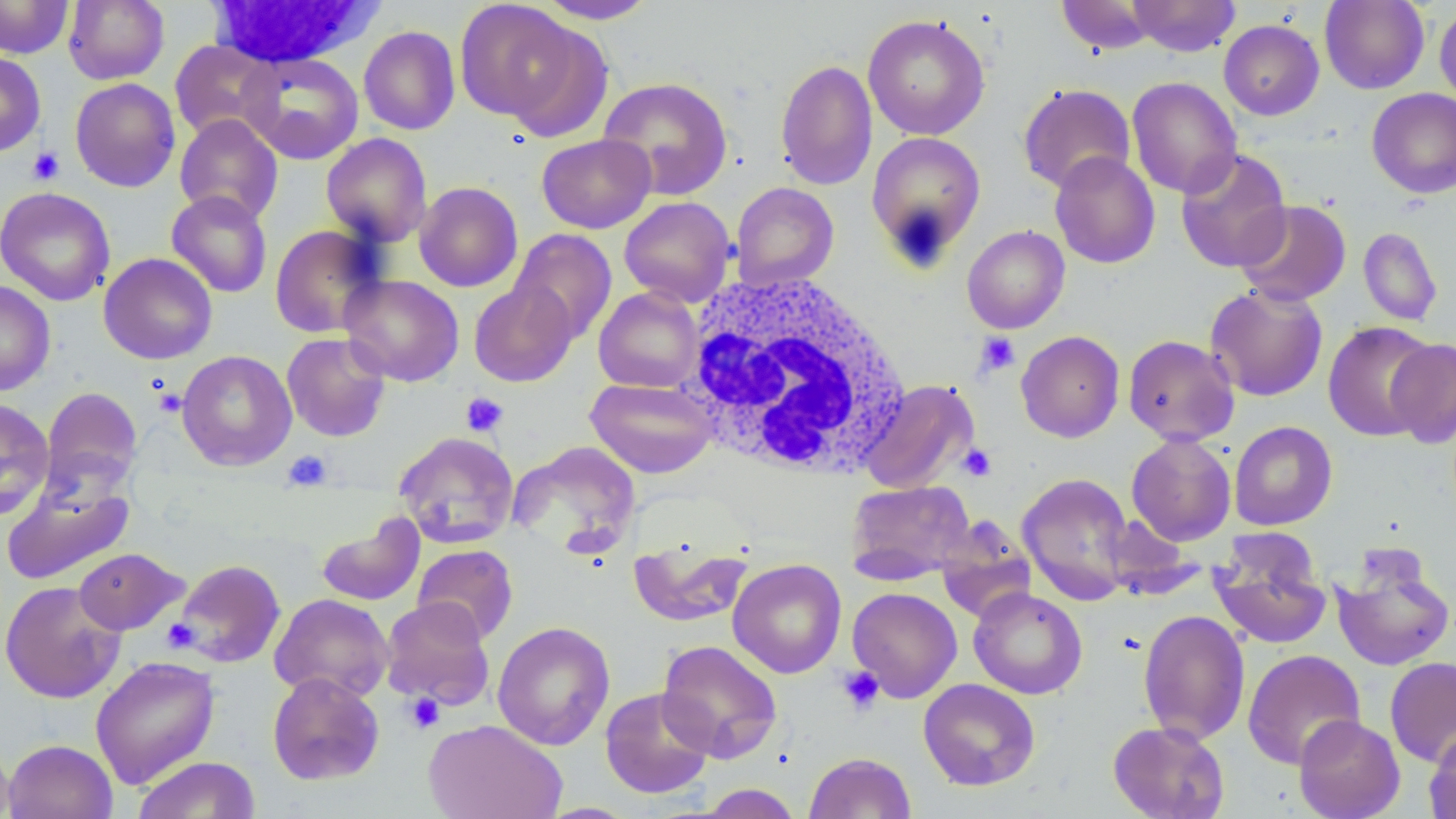

slide_level_diagnosis: no evidence of blood parasites
stain: May-Grünwald-Giemsa
magnification: 1000x
white_blood_cell_locations: 'approximate bounding boxes as named x1/y1/x2/y2 corners in pixels: (x1=206, y1=0, x2=381, y2=69), (x1=680, y1=272, x2=913, y2=480)'
uninfected_red_blood_cell_locations: 'approximate bounding boxes as named x1/y1/x2/y2 corners in pixels: (x1=0, y1=0, x2=73, y2=58), (x1=63, y1=0, x2=169, y2=85), (x1=455, y1=0, x2=581, y2=122), (x1=1056, y1=0, x2=1157, y2=55), (x1=1127, y1=0, x2=1240, y2=57), (x1=1319, y1=0, x2=1430, y2=94), (x1=535, y1=1, x2=659, y2=24), (x1=1434, y1=5, x2=1456, y2=107), (x1=863, y1=13, x2=990, y2=140), (x1=358, y1=17, x2=568, y2=128), (x1=500, y1=17, x2=614, y2=144), (x1=1219, y1=19, x2=1324, y2=120), (x1=358, y1=26, x2=460, y2=135), (x1=169, y1=40, x2=279, y2=143), (x1=0, y1=51, x2=46, y2=157), (x1=240, y1=52, x2=364, y2=164), (x1=775, y1=59, x2=878, y2=190), (x1=598, y1=76, x2=733, y2=200), (x1=69, y1=77, x2=181, y2=192), (x1=1127, y1=77, x2=1242, y2=199), (x1=1017, y1=83, x2=1136, y2=194), (x1=1366, y1=88, x2=1456, y2=198), (x1=174, y1=113, x2=283, y2=225), (x1=865, y1=130, x2=986, y2=264), (x1=321, y1=132, x2=432, y2=247), (x1=536, y1=134, x2=655, y2=233), (x1=1175, y1=148, x2=1292, y2=273), (x1=1049, y1=151, x2=1160, y2=269), (x1=414, y1=181, x2=523, y2=292), (x1=731, y1=182, x2=839, y2=290), (x1=0, y1=187, x2=115, y2=306), (x1=166, y1=190, x2=272, y2=297), (x1=619, y1=196, x2=737, y2=307), (x1=1234, y1=199, x2=1352, y2=306), (x1=270, y1=224, x2=385, y2=338), (x1=962, y1=225, x2=1070, y2=333), (x1=1358, y1=227, x2=1443, y2=326), (x1=509, y1=228, x2=618, y2=344), (x1=98, y1=253, x2=218, y2=364), (x1=339, y1=274, x2=464, y2=387), (x1=0, y1=280, x2=55, y2=396), (x1=469, y1=281, x2=578, y2=387), (x1=1205, y1=283, x2=1328, y2=402), (x1=593, y1=287, x2=704, y2=392), (x1=1322, y1=320, x2=1438, y2=442), (x1=1016, y1=331, x2=1125, y2=443), (x1=281, y1=332, x2=391, y2=442), (x1=1123, y1=334, x2=1240, y2=446), (x1=1386, y1=337, x2=1456, y2=448), (x1=177, y1=350, x2=297, y2=470), (x1=585, y1=377, x2=718, y2=478), (x1=859, y1=379, x2=979, y2=494), (x1=40, y1=386, x2=142, y2=500), (x1=0, y1=398, x2=54, y2=521), (x1=1229, y1=421, x2=1338, y2=530), (x1=393, y1=431, x2=520, y2=548), (x1=1126, y1=433, x2=1237, y2=546), (x1=508, y1=440, x2=641, y2=555), (x1=1017, y1=473, x2=1135, y2=605), (x1=846, y1=480, x2=975, y2=584), (x1=1, y1=481, x2=135, y2=586), (x1=316, y1=513, x2=425, y2=606), (x1=936, y1=518, x2=1036, y2=623), (x1=1210, y1=537, x2=1332, y2=650), (x1=629, y1=538, x2=751, y2=627), (x1=412, y1=544, x2=519, y2=644), (x1=73, y1=547, x2=188, y2=635), (x1=1331, y1=553, x2=1455, y2=672), (x1=728, y1=558, x2=847, y2=678), (x1=172, y1=559, x2=286, y2=669), (x1=0, y1=581, x2=125, y2=704), (x1=847, y1=587, x2=963, y2=703), (x1=968, y1=587, x2=1088, y2=699), (x1=269, y1=593, x2=394, y2=702), (x1=380, y1=597, x2=495, y2=710), (x1=1138, y1=609, x2=1250, y2=745), (x1=492, y1=621, x2=615, y2=750), (x1=657, y1=639, x2=782, y2=762), (x1=1242, y1=649, x2=1366, y2=770), (x1=90, y1=655, x2=220, y2=789), (x1=1384, y1=656, x2=1456, y2=767), (x1=267, y1=672, x2=385, y2=786), (x1=918, y1=678, x2=1040, y2=791), (x1=600, y1=687, x2=715, y2=799), (x1=1293, y1=714, x2=1405, y2=819), (x1=423, y1=718, x2=567, y2=819), (x1=1108, y1=720, x2=1230, y2=819), (x1=1425, y1=727, x2=1456, y2=819), (x1=4, y1=739, x2=117, y2=819), (x1=0, y1=740, x2=15, y2=818), (x1=804, y1=752, x2=917, y2=818), (x1=133, y1=756, x2=261, y2=819), (x1=695, y1=784, x2=803, y2=818), (x1=534, y1=802, x2=642, y2=818)'
field_of_view: one of a larger specimen
preparation: thin blood smear
modality: light microscopy
platelet_locations: 'approximate bounding boxes as named x1/y1/x2/y2 corners in pixels: (x1=28, y1=147, x2=64, y2=185), (x1=975, y1=331, x2=1021, y2=378), (x1=153, y1=387, x2=186, y2=419), (x1=460, y1=392, x2=509, y2=438), (x1=958, y1=444, x2=996, y2=481), (x1=283, y1=450, x2=333, y2=492), (x1=162, y1=618, x2=200, y2=653), (x1=837, y1=666, x2=885, y2=715), (x1=404, y1=692, x2=446, y2=735)'
image_size: 1456×819 pixels